Name the parasite shown.
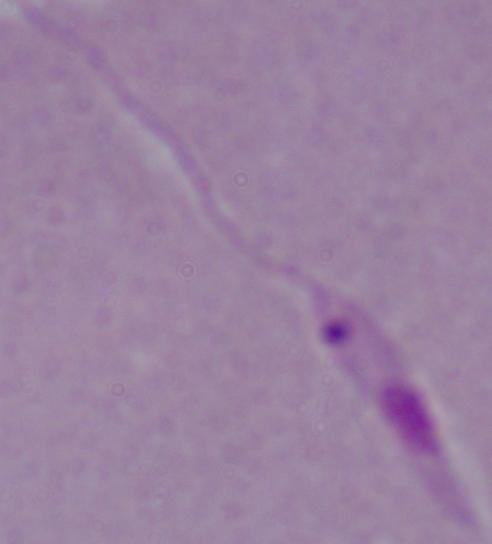

Leishmania.

modality = photomicrograph
magnification = 1000x